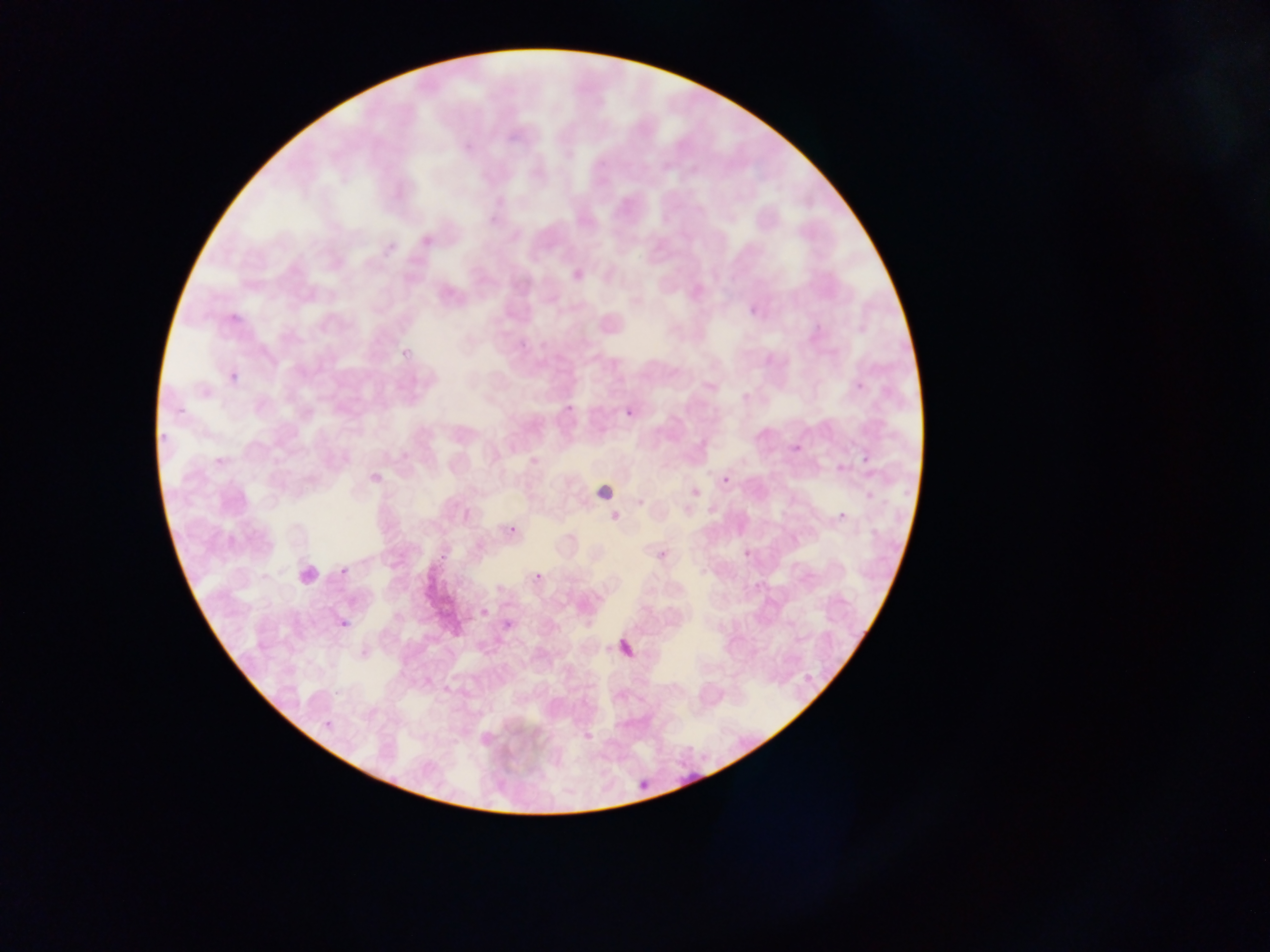
Approximate bounding boxes as (left, top, right, bottom) in pixels.
Summary:
  - Leukocyte locations: (590, 478, 622, 510)
  - Plasmodium parasite locations: (746, 302, 764, 324), (397, 337, 421, 358), (228, 360, 252, 382), (852, 379, 869, 396), (561, 397, 580, 412), (619, 402, 641, 429), (174, 405, 187, 426), (156, 424, 173, 445), (785, 433, 804, 458), (861, 445, 879, 480), (857, 451, 876, 471), (720, 472, 734, 489), (862, 488, 880, 507), (833, 507, 852, 526), (504, 520, 523, 541), (434, 545, 455, 561), (654, 546, 672, 565), (737, 546, 755, 559), (336, 562, 354, 584), (532, 568, 547, 583), (337, 614, 357, 637), (612, 634, 645, 667), (318, 719, 333, 732), (699, 750, 718, 762), (634, 776, 655, 798)
  - Field of view: single
  - Country: Ghana
  - Capture: mobile-phone photograph through a microscope
  - Preparation: thin blood smear
  - Image size: 1270×952 pixels